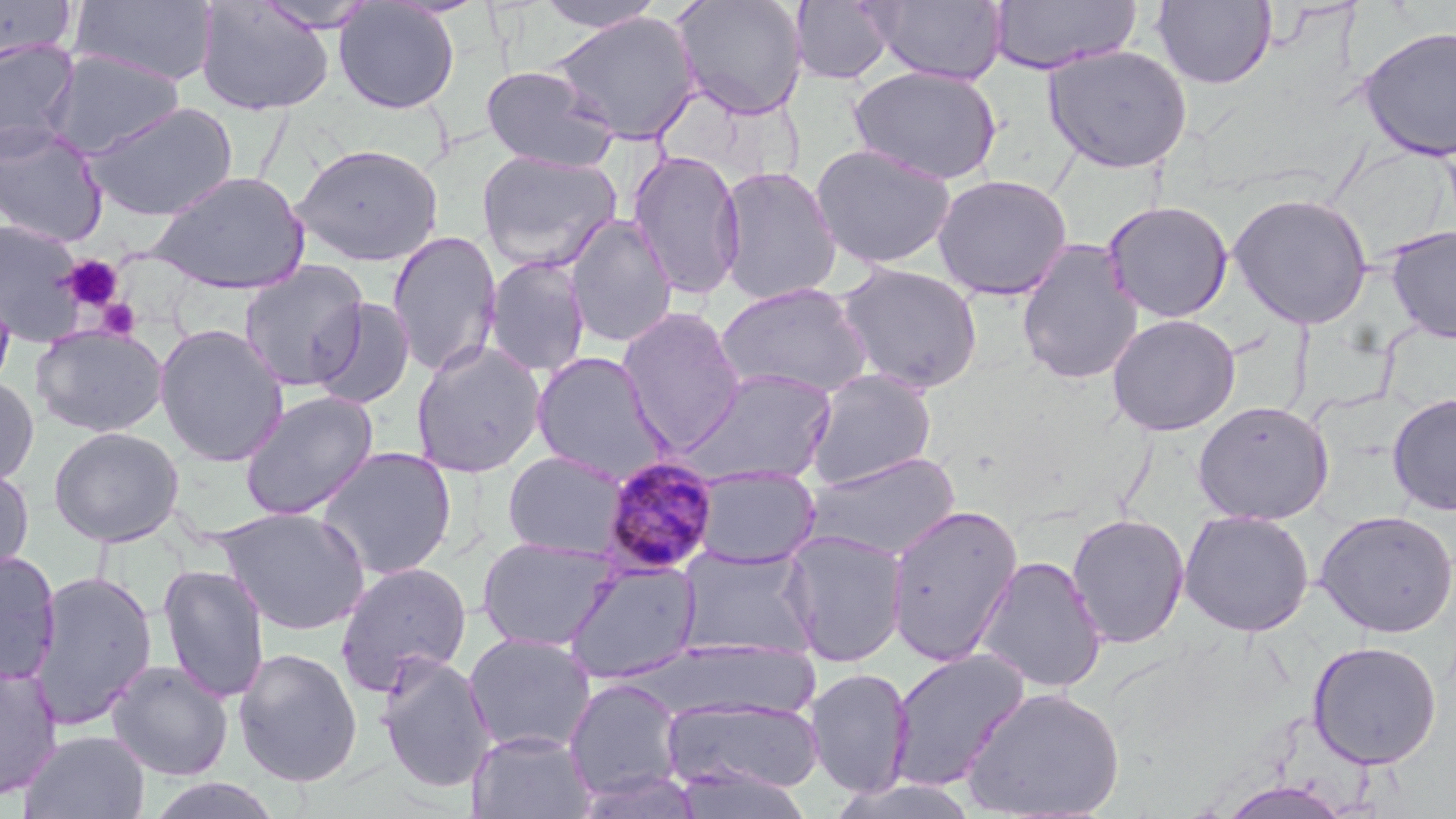

Summary:
  - Coordinate format: approximate bounding boxes as (x1,y1)-(x2,y2) corner pairs in pixels
  - Platelet locations: (61,255)-(124,312), (95,298)-(142,341)
  - Uninfected red blood cell locations: (0,0)-(76,64), (69,0)-(220,87), (673,0)-(807,121), (869,0)-(1009,85), (1152,0)-(1277,90), (195,1)-(335,116), (254,1)-(382,33), (333,1)-(460,114), (534,1)-(666,33), (790,1)-(897,85), (988,1)-(1142,74), (548,10)-(702,144), (1357,25)-(1456,162), (0,38)-(80,158), (1043,43)-(1193,174), (44,48)-(187,158), (480,64)-(617,172), (847,65)-(1003,185), (83,101)-(239,221), (0,122)-(109,247), (291,143)-(444,266), (810,143)-(958,271), (476,150)-(622,271), (626,150)-(746,300), (715,165)-(842,306), (146,170)-(310,295), (931,173)-(1073,300), (1227,192)-(1373,329), (1102,200)-(1234,322), (565,215)-(678,349), (0,219)-(90,347), (1385,226)-(1456,343), (386,230)-(503,377), (1015,239)-(1145,386), (484,256)-(591,378), (238,260)-(369,391), (834,260)-(984,395), (714,282)-(874,400), (309,297)-(416,410), (616,306)-(747,453), (1106,313)-(1240,436), (31,324)-(169,437), (154,324)-(289,467), (410,340)-(548,478), (530,351)-(674,484), (678,367)-(839,488), (803,369)-(937,489), (0,375)-(39,487), (239,390)-(379,520), (1387,393)-(1456,516), (1192,400)-(1333,525), (48,426)-(184,547), (315,446)-(458,580), (802,450)-(962,561), (502,451)-(630,559), (0,464)-(34,581), (691,465)-(820,568), (887,502)-(1023,666), (216,507)-(371,635), (1314,509)-(1456,637), (1178,510)-(1314,637), (1066,513)-(1190,649), (781,530)-(909,668), (476,536)-(623,652), (677,545)-(820,660), (0,550)-(62,684), (974,555)-(1108,693), (334,561)-(472,695), (563,561)-(702,685), (157,563)-(270,703), (31,570)-(157,730), (463,633)-(597,755), (1306,640)-(1442,768), (232,646)-(363,787), (887,648)-(1030,792), (376,654)-(496,793), (107,660)-(233,780), (0,662)-(63,801), (803,666)-(914,798), (564,677)-(686,804), (962,686)-(1125,819), (661,694)-(825,799), (19,729)-(151,819), (466,730)-(595,819), (826,774)-(982,819), (143,777)-(287,819), (1221,780)-(1353,819)
  - Plasmodium malariae-infected red blood cell locations: (600,456)-(720,576)
  - Slide-level diagnosis: Plasmodium malariae
  - Magnification: 1000x
  - Stain: May-Grünwald-Giemsa
  - Image size: 1456×819 pixels
  - Modality: light microscopy
  - Field of view: single
  - Preparation: thin blood smear